Identify the blood parasite species.
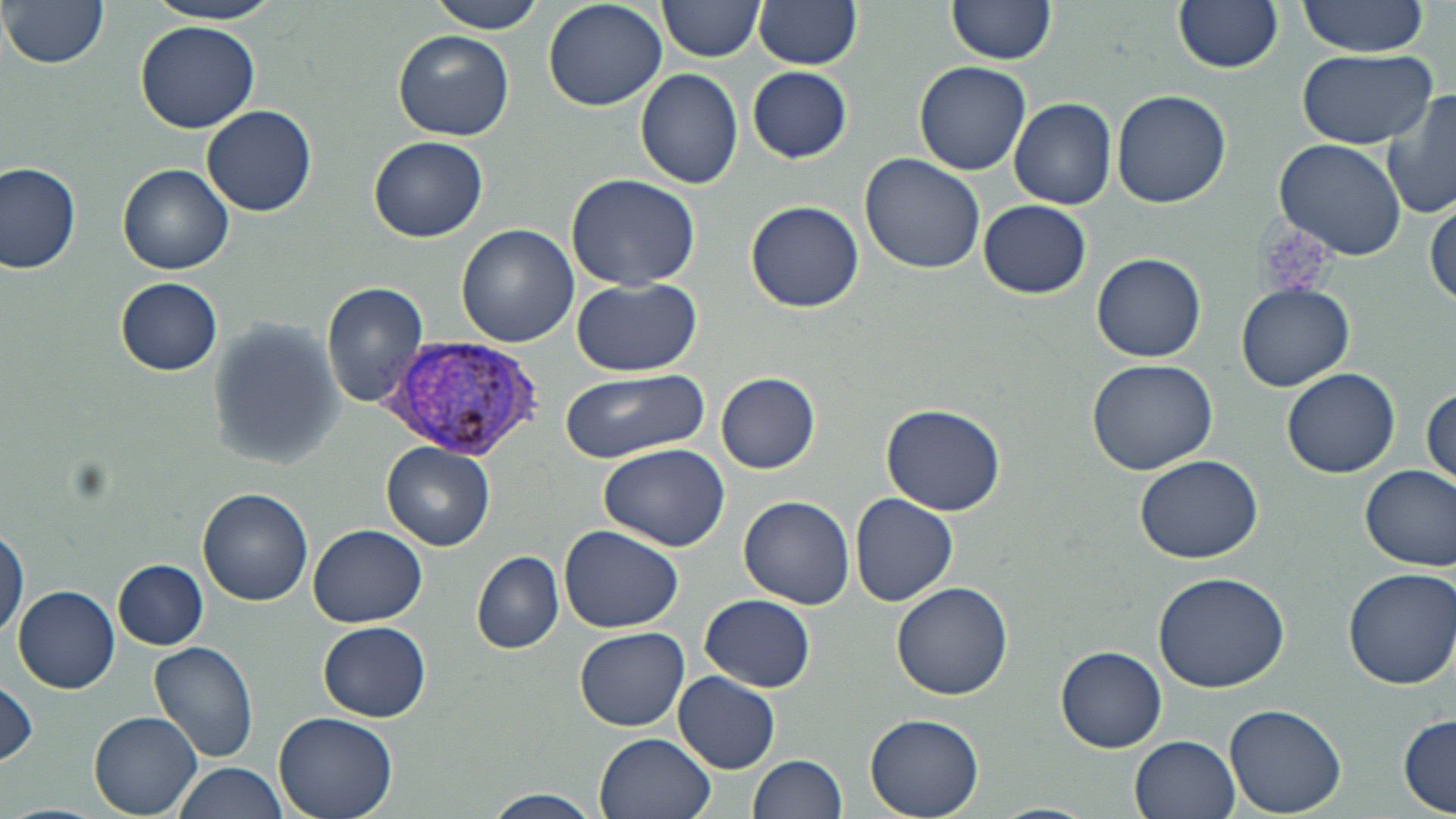

Plasmodium vivax.

field of view = one of a larger specimen
preparation = thin blood film
Plasmodium vivax-infected red blood cell locations = approximate bounding boxes as [x1, y1, x2, y2] in pixels: [389, 336, 548, 462]
image size = 1456×819 pixels
magnification = 1000x
modality = optical microscopy
uninfected red blood cell locations = approximate bounding boxes as [x1, y1, x2, y2] in pixels: [5, 0, 110, 70], [147, 0, 283, 25], [428, 0, 547, 34], [658, 0, 763, 61], [752, 0, 863, 69], [949, 0, 1056, 66], [1174, 0, 1284, 73], [1296, 0, 1427, 56], [542, 1, 668, 112], [135, 20, 259, 132], [394, 30, 512, 140], [1298, 48, 1436, 147], [914, 62, 1031, 176], [748, 67, 853, 161], [635, 68, 743, 189], [1384, 87, 1456, 220], [1111, 90, 1231, 208], [1009, 97, 1116, 210], [202, 105, 317, 216], [369, 136, 488, 241], [1275, 138, 1407, 260], [859, 153, 987, 277], [0, 160, 82, 274], [118, 163, 234, 274], [565, 173, 700, 290], [1428, 196, 1456, 308], [978, 200, 1092, 298], [744, 201, 865, 313], [456, 225, 579, 348], [1092, 251, 1208, 362], [114, 277, 223, 376], [573, 277, 701, 377], [323, 280, 430, 408], [1237, 282, 1355, 391], [207, 321, 345, 467], [1086, 358, 1219, 475], [1283, 366, 1401, 477], [558, 370, 708, 463], [716, 371, 821, 473], [1422, 387, 1455, 492], [882, 403, 1006, 515], [597, 441, 730, 549], [382, 442, 495, 550], [1134, 453, 1263, 565], [1360, 463, 1456, 572], [198, 489, 314, 607], [849, 492, 957, 606], [738, 495, 855, 608], [558, 523, 685, 634], [308, 524, 427, 627], [0, 526, 26, 639], [471, 550, 564, 653], [113, 560, 209, 649], [1343, 567, 1456, 689], [1152, 571, 1291, 693], [890, 580, 1013, 699], [14, 584, 119, 692], [701, 594, 815, 693], [319, 622, 432, 721], [574, 627, 690, 732], [149, 642, 260, 764], [1056, 647, 1167, 752], [674, 672, 780, 773], [0, 677, 38, 770], [1224, 704, 1347, 818], [273, 711, 398, 819], [89, 712, 202, 818], [863, 713, 984, 819], [1397, 715, 1456, 814], [594, 733, 717, 819], [1130, 734, 1241, 818], [749, 755, 847, 819], [174, 762, 289, 818], [480, 790, 606, 819], [989, 801, 1101, 819]
stain = May-Grünwald-Giemsa